State which parasite is depicted.
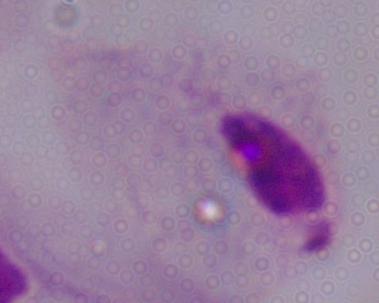
This is a trichomonad.

Micrograph. Captured at 1000x magnification.